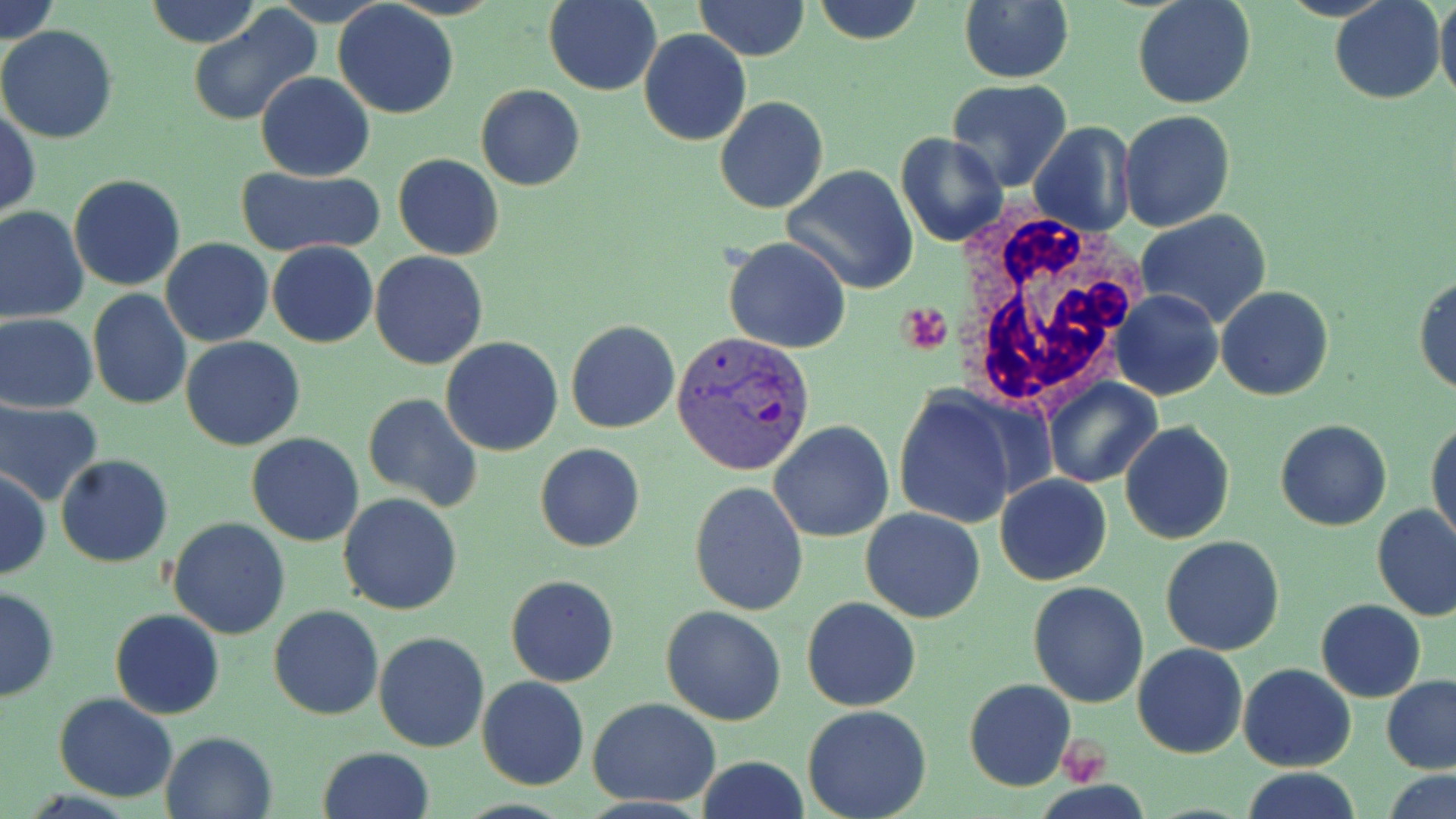
Summary:
  - Coordinate format: approximate bounding boxes as named x1/y1/x2/y2 corners in pixels
  - White blood cell locations: (x1=952, y1=215, x2=1143, y2=413)
  - Plasmodium vivax-infected red blood cell locations: (x1=673, y1=331, x2=816, y2=475)
  - Uninfected red blood cell locations: (x1=1, y1=0, x2=61, y2=46), (x1=142, y1=0, x2=262, y2=47), (x1=544, y1=0, x2=661, y2=95), (x1=695, y1=0, x2=810, y2=61), (x1=811, y1=0, x2=925, y2=45), (x1=1132, y1=0, x2=1256, y2=109), (x1=1329, y1=0, x2=1447, y2=105), (x1=1436, y1=0, x2=1456, y2=109), (x1=960, y1=1, x2=1074, y2=84), (x1=333, y1=2, x2=458, y2=118), (x1=187, y1=8, x2=320, y2=127), (x1=0, y1=26, x2=118, y2=144), (x1=640, y1=29, x2=750, y2=145), (x1=255, y1=72, x2=375, y2=181), (x1=945, y1=81, x2=1074, y2=195), (x1=475, y1=84, x2=585, y2=191), (x1=714, y1=96, x2=829, y2=214), (x1=1, y1=107, x2=40, y2=220), (x1=1118, y1=109, x2=1236, y2=230), (x1=1028, y1=120, x2=1136, y2=237), (x1=896, y1=132, x2=1008, y2=247), (x1=393, y1=153, x2=504, y2=260), (x1=783, y1=164, x2=919, y2=294), (x1=238, y1=167, x2=380, y2=256), (x1=68, y1=174, x2=187, y2=291), (x1=0, y1=207, x2=89, y2=324), (x1=1134, y1=211, x2=1276, y2=332), (x1=161, y1=237, x2=273, y2=347), (x1=723, y1=237, x2=851, y2=354), (x1=268, y1=240, x2=378, y2=349), (x1=369, y1=250, x2=488, y2=369), (x1=1415, y1=273, x2=1456, y2=397), (x1=1216, y1=285, x2=1334, y2=401), (x1=87, y1=288, x2=192, y2=409), (x1=1113, y1=290, x2=1223, y2=401), (x1=1, y1=313, x2=99, y2=412), (x1=566, y1=321, x2=679, y2=435), (x1=181, y1=337, x2=306, y2=452), (x1=441, y1=337, x2=564, y2=456), (x1=1041, y1=376, x2=1162, y2=490), (x1=892, y1=389, x2=1026, y2=531), (x1=362, y1=392, x2=483, y2=511), (x1=0, y1=399, x2=102, y2=506), (x1=1275, y1=419, x2=1393, y2=531), (x1=1427, y1=419, x2=1456, y2=547), (x1=769, y1=420, x2=894, y2=541), (x1=1118, y1=421, x2=1235, y2=545), (x1=246, y1=432, x2=363, y2=546), (x1=535, y1=443, x2=644, y2=552), (x1=56, y1=454, x2=172, y2=567), (x1=0, y1=469, x2=49, y2=580), (x1=994, y1=475, x2=1112, y2=586), (x1=689, y1=481, x2=811, y2=617), (x1=339, y1=493, x2=463, y2=615), (x1=1372, y1=505, x2=1456, y2=621), (x1=862, y1=508, x2=985, y2=623), (x1=168, y1=518, x2=292, y2=639), (x1=1161, y1=535, x2=1286, y2=656), (x1=506, y1=574, x2=619, y2=686), (x1=1028, y1=581, x2=1149, y2=706), (x1=0, y1=587, x2=59, y2=701), (x1=801, y1=595, x2=921, y2=711), (x1=1316, y1=599, x2=1425, y2=702), (x1=268, y1=604, x2=385, y2=720), (x1=660, y1=606, x2=787, y2=726), (x1=109, y1=609, x2=224, y2=720), (x1=373, y1=631, x2=489, y2=754), (x1=1132, y1=642, x2=1248, y2=759), (x1=1239, y1=664, x2=1355, y2=772), (x1=476, y1=675, x2=589, y2=790), (x1=1381, y1=676, x2=1456, y2=774), (x1=963, y1=678, x2=1076, y2=791), (x1=54, y1=692, x2=178, y2=801), (x1=586, y1=697, x2=721, y2=809), (x1=801, y1=704, x2=933, y2=819), (x1=160, y1=729, x2=278, y2=819), (x1=318, y1=745, x2=434, y2=819), (x1=694, y1=757, x2=810, y2=818), (x1=1238, y1=768, x2=1361, y2=819), (x1=1380, y1=768, x2=1456, y2=819)
  - Platelet locations: (x1=898, y1=303, x2=952, y2=355), (x1=1056, y1=738, x2=1111, y2=783)
  - Slide-level diagnosis: Plasmodium vivax
  - Preparation: thin blood smear
  - Modality: optical microscopy
  - Stain: May-Grünwald-Giemsa
  - Field of view: single
  - Image size: 1456×819 pixels
  - Magnification: 1000x